Assess this cell for malaria.
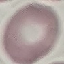

It is uninfected.

{
  "image_type": "automatically extracted cell patch, resized to 64 × 64 pixels",
  "capture": "smartphone camera at the microscope eyepiece",
  "stain": "Giemsa",
  "preparation": "thin smear"
}